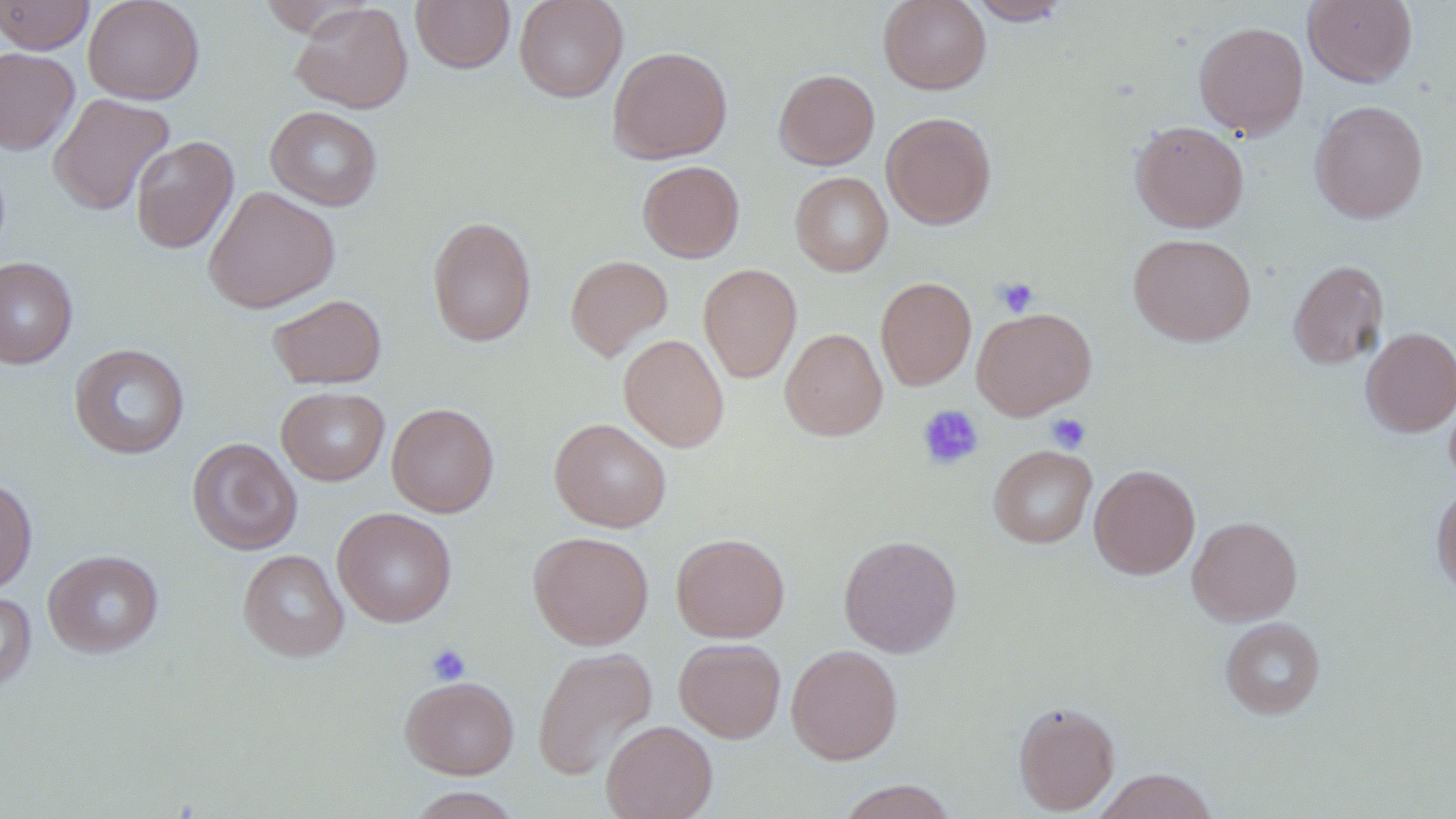
Summary:
  - Coordinate format: approximate bounding boxes as named x1/y1/x2/y2 corners in pixels
  - Platelet locations: (x1=993, y1=277, x2=1038, y2=318), (x1=917, y1=404, x2=984, y2=471), (x1=1047, y1=413, x2=1091, y2=453), (x1=426, y1=643, x2=471, y2=686)
  - Uninfected red blood cell locations: (x1=0, y1=0, x2=95, y2=54), (x1=83, y1=0, x2=204, y2=104), (x1=411, y1=0, x2=515, y2=73), (x1=514, y1=0, x2=628, y2=102), (x1=878, y1=0, x2=991, y2=94), (x1=967, y1=0, x2=1072, y2=25), (x1=1303, y1=0, x2=1418, y2=87), (x1=291, y1=3, x2=413, y2=114), (x1=1194, y1=21, x2=1309, y2=139), (x1=608, y1=46, x2=732, y2=164), (x1=0, y1=47, x2=80, y2=154), (x1=774, y1=69, x2=879, y2=170), (x1=49, y1=93, x2=174, y2=216), (x1=1310, y1=100, x2=1429, y2=224), (x1=265, y1=106, x2=383, y2=211), (x1=881, y1=112, x2=996, y2=229), (x1=1130, y1=120, x2=1249, y2=233), (x1=130, y1=135, x2=239, y2=254), (x1=637, y1=160, x2=744, y2=262), (x1=790, y1=172, x2=893, y2=276), (x1=203, y1=186, x2=340, y2=313), (x1=427, y1=216, x2=537, y2=347), (x1=1128, y1=233, x2=1256, y2=347), (x1=565, y1=255, x2=673, y2=361), (x1=0, y1=257, x2=78, y2=368), (x1=1288, y1=260, x2=1389, y2=369), (x1=698, y1=264, x2=801, y2=382), (x1=875, y1=277, x2=976, y2=390), (x1=268, y1=294, x2=387, y2=389), (x1=972, y1=307, x2=1096, y2=419), (x1=1360, y1=327, x2=1456, y2=436), (x1=780, y1=328, x2=887, y2=441), (x1=618, y1=333, x2=729, y2=452), (x1=69, y1=343, x2=190, y2=459), (x1=276, y1=387, x2=390, y2=486), (x1=387, y1=403, x2=499, y2=518), (x1=549, y1=418, x2=671, y2=532), (x1=187, y1=437, x2=302, y2=555), (x1=988, y1=445, x2=1097, y2=548), (x1=1089, y1=464, x2=1200, y2=579), (x1=0, y1=477, x2=37, y2=595), (x1=1431, y1=482, x2=1456, y2=598), (x1=332, y1=507, x2=457, y2=627), (x1=1187, y1=515, x2=1302, y2=625), (x1=528, y1=531, x2=654, y2=649), (x1=671, y1=533, x2=790, y2=642), (x1=839, y1=534, x2=962, y2=657), (x1=238, y1=549, x2=349, y2=662), (x1=43, y1=550, x2=164, y2=658), (x1=0, y1=592, x2=37, y2=692), (x1=1220, y1=617, x2=1325, y2=719), (x1=674, y1=637, x2=786, y2=743), (x1=787, y1=644, x2=903, y2=764), (x1=532, y1=646, x2=657, y2=780), (x1=400, y1=675, x2=519, y2=779), (x1=1013, y1=700, x2=1120, y2=815), (x1=602, y1=720, x2=718, y2=819), (x1=1093, y1=768, x2=1218, y2=819), (x1=835, y1=780, x2=960, y2=819), (x1=405, y1=787, x2=522, y2=818)
  - Slide-level diagnosis: negative for blood parasites
  - Stain: May-Grünwald-Giemsa
  - Image size: 1456×819 pixels
  - Field of view: single
  - Preparation: thin blood film
  - Magnification: 1000x
  - Modality: optical microscopy